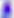

Photomicrograph. 400x magnification. Toxoplasma gondii is shown.